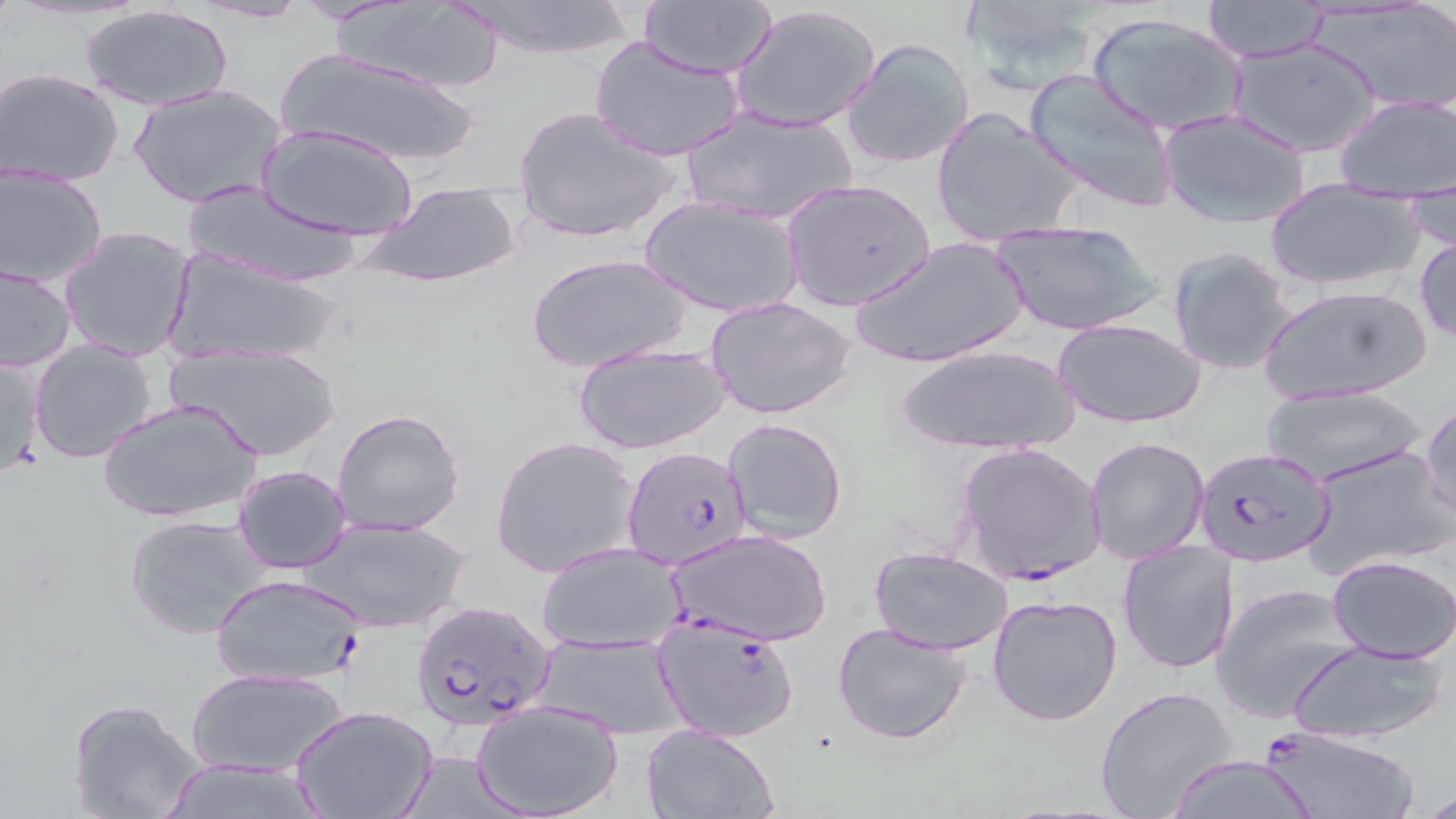 Approximate bounding boxes as named x1/y1/x2/y2 corners in pixels. Plasmodium falciparum-infected red blood cell locations: (x1=956, y1=442, x2=1105, y2=587), (x1=621, y1=446, x2=753, y2=571), (x1=1195, y1=448, x2=1335, y2=568), (x1=209, y1=572, x2=370, y2=689), (x1=408, y1=600, x2=561, y2=735), (x1=650, y1=611, x2=801, y2=744), (x1=1258, y1=727, x2=1419, y2=819). Uninfected red blood cell locations: (x1=639, y1=1, x2=778, y2=78), (x1=960, y1=1, x2=1103, y2=97), (x1=1200, y1=1, x2=1331, y2=63), (x1=1309, y1=1, x2=1456, y2=111), (x1=448, y1=2, x2=640, y2=61), (x1=333, y1=3, x2=507, y2=92), (x1=731, y1=3, x2=883, y2=134), (x1=80, y1=5, x2=234, y2=113), (x1=1085, y1=9, x2=1249, y2=137), (x1=588, y1=36, x2=745, y2=162), (x1=1227, y1=37, x2=1381, y2=157), (x1=842, y1=38, x2=976, y2=170), (x1=277, y1=49, x2=484, y2=168), (x1=1, y1=67, x2=126, y2=187), (x1=1024, y1=69, x2=1178, y2=214), (x1=129, y1=82, x2=286, y2=209), (x1=1334, y1=93, x2=1455, y2=201), (x1=514, y1=105, x2=681, y2=244), (x1=679, y1=106, x2=858, y2=226), (x1=932, y1=107, x2=1083, y2=248), (x1=1159, y1=109, x2=1312, y2=229), (x1=258, y1=125, x2=417, y2=241), (x1=1, y1=166, x2=107, y2=287), (x1=781, y1=178, x2=936, y2=311), (x1=364, y1=180, x2=520, y2=289), (x1=1404, y1=181, x2=1454, y2=257), (x1=1264, y1=182, x2=1423, y2=293), (x1=182, y1=183, x2=369, y2=288), (x1=638, y1=195, x2=803, y2=318), (x1=987, y1=218, x2=1161, y2=334), (x1=59, y1=224, x2=197, y2=361), (x1=851, y1=236, x2=1029, y2=370), (x1=1416, y1=236, x2=1456, y2=342), (x1=165, y1=245, x2=343, y2=366), (x1=1166, y1=246, x2=1297, y2=376), (x1=527, y1=253, x2=692, y2=372), (x1=0, y1=261, x2=76, y2=374), (x1=1259, y1=283, x2=1433, y2=405), (x1=706, y1=296, x2=858, y2=420), (x1=1053, y1=317, x2=1206, y2=428), (x1=29, y1=339, x2=160, y2=464), (x1=168, y1=339, x2=344, y2=462), (x1=573, y1=340, x2=729, y2=456), (x1=893, y1=343, x2=1083, y2=457), (x1=0, y1=353, x2=48, y2=480), (x1=1258, y1=384, x2=1427, y2=487), (x1=99, y1=397, x2=263, y2=525), (x1=1421, y1=401, x2=1455, y2=524), (x1=332, y1=409, x2=465, y2=538), (x1=722, y1=418, x2=848, y2=544), (x1=492, y1=435, x2=641, y2=580), (x1=1085, y1=436, x2=1211, y2=566), (x1=1302, y1=444, x2=1454, y2=578), (x1=231, y1=466, x2=354, y2=572), (x1=122, y1=513, x2=276, y2=639), (x1=300, y1=514, x2=470, y2=633), (x1=669, y1=529, x2=834, y2=647), (x1=1117, y1=539, x2=1240, y2=673), (x1=536, y1=543, x2=687, y2=653), (x1=869, y1=547, x2=1015, y2=654), (x1=1326, y1=554, x2=1456, y2=662), (x1=1210, y1=581, x2=1363, y2=724), (x1=987, y1=593, x2=1122, y2=726), (x1=833, y1=623, x2=974, y2=746), (x1=532, y1=631, x2=685, y2=738), (x1=1285, y1=640, x2=1450, y2=745), (x1=188, y1=667, x2=347, y2=778), (x1=1094, y1=685, x2=1239, y2=819), (x1=67, y1=698, x2=206, y2=819), (x1=473, y1=699, x2=623, y2=818), (x1=290, y1=705, x2=438, y2=819), (x1=642, y1=725, x2=778, y2=819), (x1=1166, y1=755, x2=1318, y2=819), (x1=156, y1=759, x2=335, y2=818). Slide-level diagnosis: Plasmodium falciparum. 1000x magnification. Thin blood film. Light microscopy. May-Grünwald-Giemsa-stained preparation. Image is 1456×819 pixels. One field of a larger specimen.